Assess this cell for malaria.
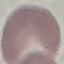
It is uninfected.

Summary:
  - Stain: Giemsa
  - Preparation: thin smear
  - Image type: cell patch, automatically extracted from a larger field of view and resized to 64 × 64 pixels
  - Capture: smartphone through the microscope eyepiece